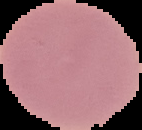
Summary:
  - Result: negative for malaria parasites
  - Image size: 142×130 pixels
  - Preparation: thin blood film
  - Image type: segmented cell region on a black background